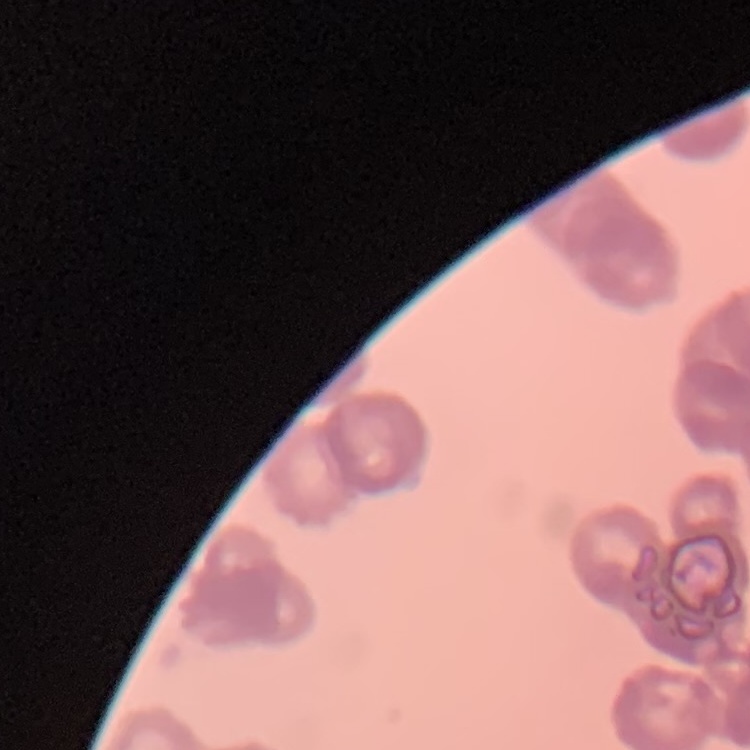

red blood cell morphology = rouleaux formation
stain = Field's or Giemsa
image type = square crop of a larger photomicrograph
preparation = thin blood film